Describe the morphology of the red blood cells.
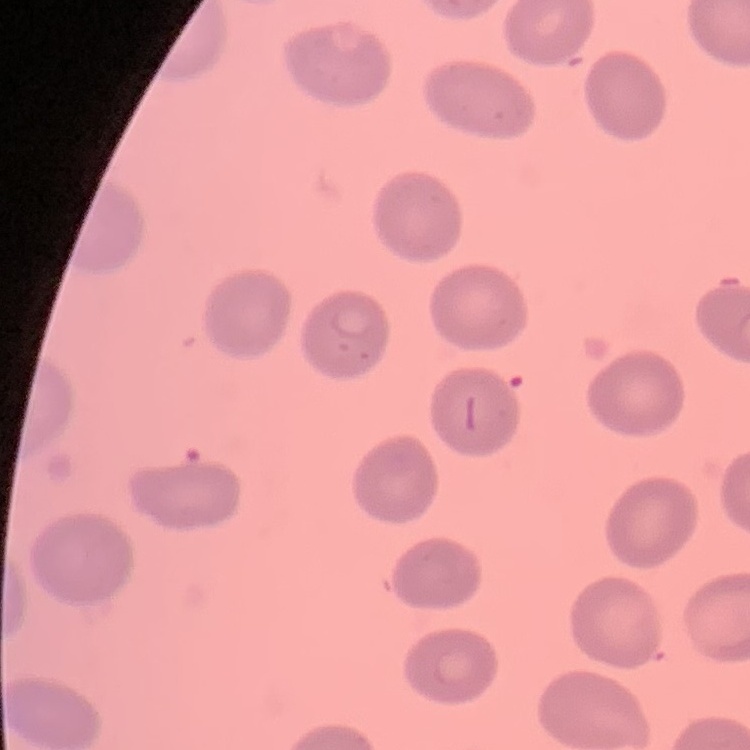
No rouleaux formation.

One tile cut from a larger photomicrograph. Stained with either Field's or Giemsa. Thin blood film.